State the preparation type.
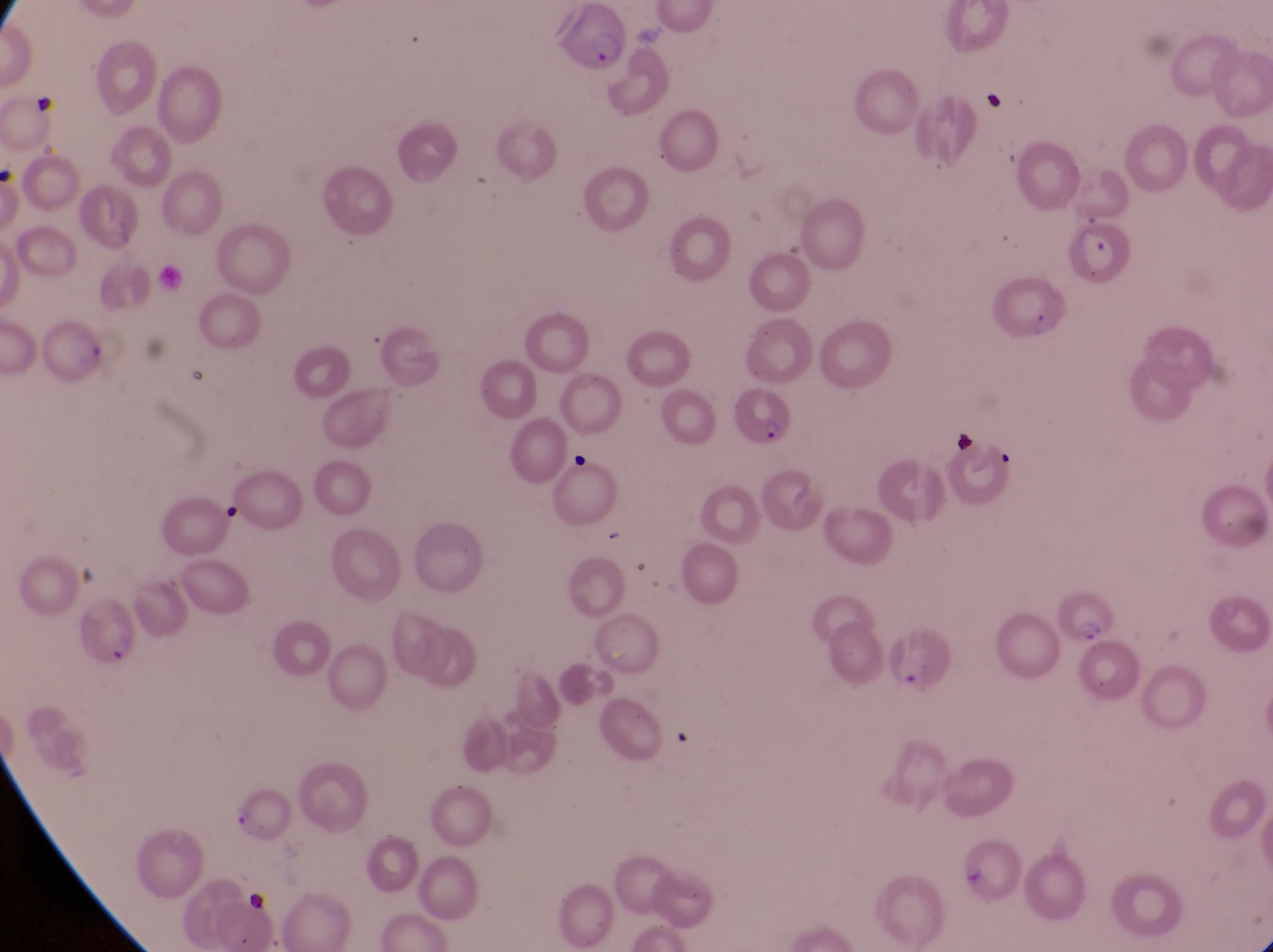

Thin blood smear.

parasitised_red_blood_cell_locations: 'approximate bounding boxes as {left, top, right, bottom} in pixels: {1069, 223, 1141, 297}, {736, 390, 794, 448}, {1055, 586, 1122, 646}'
capture: smartphone photograph through the eyepiece of an Olympus CX-23 microscope
magnification: 1000x
country: Uganda
image_size: 1273×952 pixels
field_of_view: single